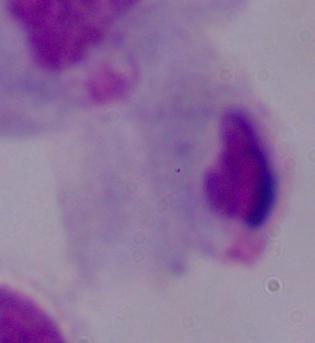

1000x magnification. Micrograph. A trichomonad is seen.